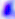

Micrograph. Captured at 400x magnification. Toxoplasma gondii is shown.